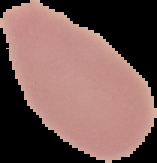
image size = 157×163 pixels
image type = segmented cell region on a black background
result = negative for malaria parasites
preparation = thin blood film